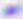
Summary:
  - Identification: Toxoplasma gondii
  - Modality: micrograph
  - Magnification: 400x